Locate every uninfected red blood cell.
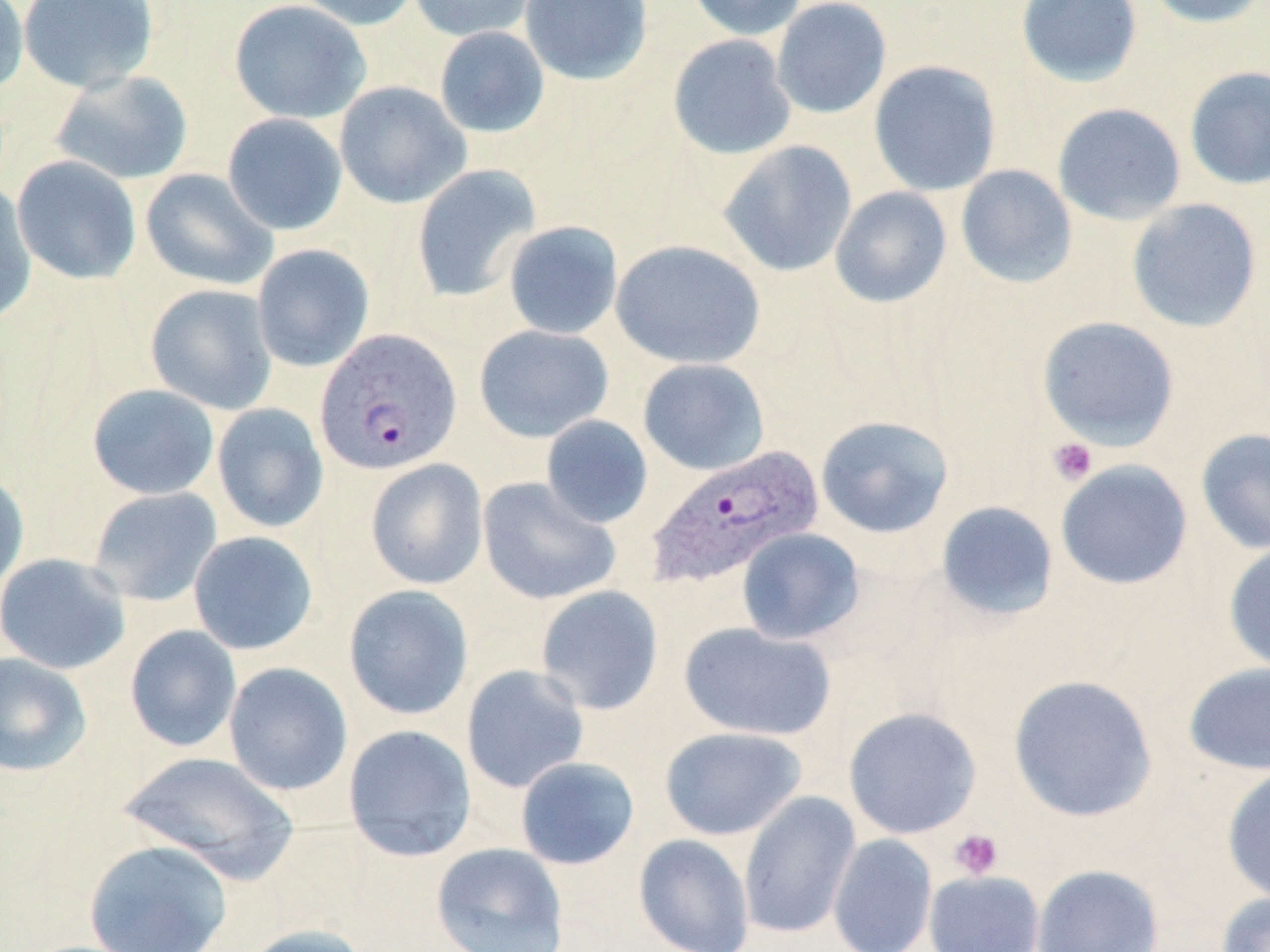

Approximate bounding boxes as named x1/y1/x2/y2 corners in pixels.
Uninfected red blood cells: (x1=0, y1=0, x2=30, y2=98), (x1=17, y1=0, x2=160, y2=93), (x1=229, y1=0, x2=371, y2=124), (x1=287, y1=0, x2=421, y2=31), (x1=407, y1=0, x2=541, y2=42), (x1=519, y1=0, x2=653, y2=85), (x1=684, y1=0, x2=808, y2=41), (x1=1015, y1=0, x2=1143, y2=87), (x1=1142, y1=0, x2=1268, y2=28), (x1=771, y1=1, x2=892, y2=119), (x1=434, y1=26, x2=550, y2=138), (x1=667, y1=34, x2=797, y2=160), (x1=868, y1=60, x2=1002, y2=197), (x1=1184, y1=66, x2=1270, y2=190), (x1=51, y1=71, x2=194, y2=186), (x1=334, y1=81, x2=471, y2=209), (x1=1051, y1=102, x2=1187, y2=225), (x1=222, y1=113, x2=348, y2=235), (x1=717, y1=139, x2=858, y2=278), (x1=11, y1=155, x2=142, y2=285), (x1=411, y1=164, x2=542, y2=302), (x1=955, y1=164, x2=1078, y2=288), (x1=140, y1=168, x2=277, y2=291), (x1=0, y1=182, x2=37, y2=326), (x1=829, y1=186, x2=952, y2=308), (x1=1126, y1=198, x2=1262, y2=332), (x1=502, y1=220, x2=623, y2=340), (x1=611, y1=239, x2=766, y2=370), (x1=252, y1=244, x2=375, y2=372), (x1=145, y1=284, x2=278, y2=415), (x1=1036, y1=316, x2=1180, y2=451), (x1=474, y1=324, x2=614, y2=443), (x1=637, y1=358, x2=771, y2=475), (x1=87, y1=384, x2=220, y2=500), (x1=211, y1=403, x2=329, y2=533), (x1=541, y1=415, x2=653, y2=529), (x1=815, y1=415, x2=954, y2=539), (x1=1196, y1=427, x2=1270, y2=554), (x1=365, y1=458, x2=489, y2=590), (x1=1055, y1=459, x2=1193, y2=591), (x1=0, y1=469, x2=30, y2=597), (x1=477, y1=477, x2=622, y2=605), (x1=87, y1=487, x2=222, y2=607), (x1=935, y1=500, x2=1060, y2=623), (x1=736, y1=528, x2=865, y2=645), (x1=188, y1=531, x2=319, y2=656), (x1=1223, y1=541, x2=1270, y2=674), (x1=1, y1=552, x2=131, y2=675), (x1=343, y1=584, x2=475, y2=721), (x1=534, y1=585, x2=664, y2=716), (x1=679, y1=622, x2=837, y2=742), (x1=124, y1=624, x2=242, y2=752), (x1=0, y1=652, x2=93, y2=777), (x1=1183, y1=661, x2=1270, y2=776), (x1=223, y1=662, x2=354, y2=796), (x1=461, y1=664, x2=591, y2=793), (x1=1008, y1=674, x2=1158, y2=822), (x1=842, y1=706, x2=981, y2=840), (x1=342, y1=724, x2=477, y2=863), (x1=659, y1=726, x2=808, y2=841), (x1=117, y1=750, x2=300, y2=882), (x1=515, y1=756, x2=640, y2=870), (x1=1222, y1=765, x2=1270, y2=904), (x1=738, y1=791, x2=861, y2=940), (x1=827, y1=833, x2=938, y2=952), (x1=633, y1=834, x2=755, y2=952), (x1=84, y1=839, x2=233, y2=952), (x1=431, y1=842, x2=569, y2=952), (x1=1031, y1=863, x2=1164, y2=952), (x1=923, y1=869, x2=1045, y2=952), (x1=1216, y1=891, x2=1270, y2=952), (x1=240, y1=924, x2=370, y2=952).

Platelet locations: (x1=1047, y1=437, x2=1098, y2=485), (x1=949, y1=828, x2=1003, y2=879). Plasmodium vivax-infected red blood cell locations: (x1=313, y1=330, x2=459, y2=476), (x1=644, y1=448, x2=823, y2=590). Slide-level diagnosis: Plasmodium vivax. Thin blood film. Single field of view. Image is 1270×952 pixels. Light microscopy. May-Grünwald-Giemsa-stained preparation. Captured at 1000x magnification.